Outline each blood parasite and name the species.
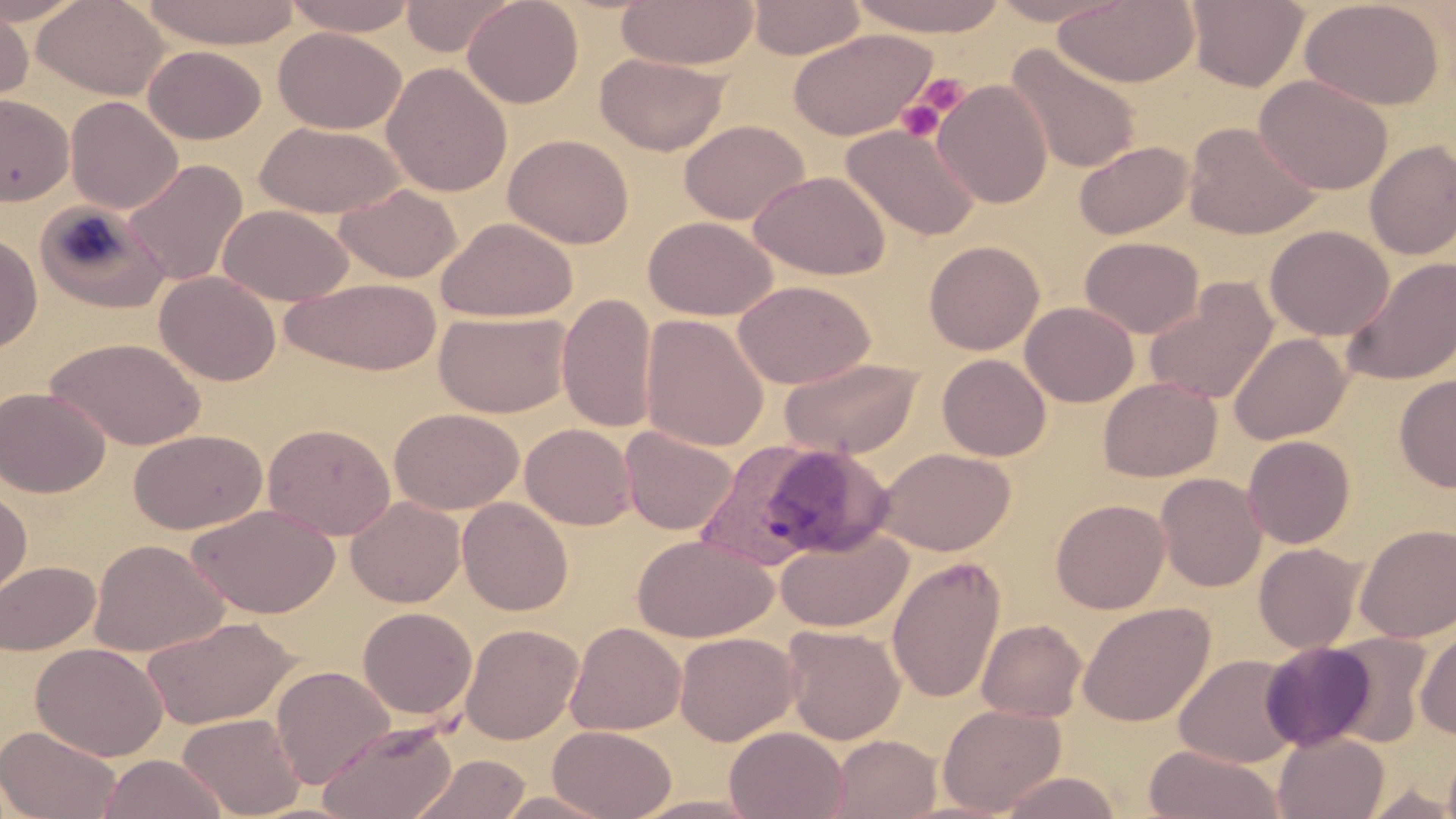
Approximate bounding boxes as (x1,y1)-(x2,y2) corner pairs in pixels.
Plasmodium vivax-infected red blood cells: (694,439)-(872,571).
No Plasmodium falciparum, Plasmodium ovale, Plasmodium malariae, Babesia divergens, or Trypanosoma brucei observed.

Summary:
  - Uninfected red blood cell locations: (0,0)-(88,25), (33,0)-(170,101), (140,0)-(303,48), (280,0)-(419,36), (401,0)-(516,56), (462,0)-(583,108), (616,0)-(759,70), (747,0)-(866,59), (847,0)-(1011,37), (985,0)-(1131,26), (1052,0)-(1200,87), (1186,0)-(1308,90), (1300,0)-(1445,110), (0,8)-(33,110), (274,27)-(406,134), (787,28)-(938,142), (1006,44)-(1142,174), (143,45)-(266,144), (596,53)-(731,155), (382,62)-(512,197), (1255,75)-(1393,194), (933,80)-(1053,209), (0,94)-(74,206), (65,96)-(182,214), (679,119)-(809,224), (254,121)-(406,218), (1183,121)-(1322,239), (840,123)-(983,241), (504,134)-(634,248), (1073,140)-(1193,240), (1364,141)-(1456,260), (123,159)-(248,287), (749,170)-(891,280), (333,183)-(463,283), (34,201)-(169,313), (218,204)-(354,306), (643,216)-(776,320), (435,217)-(578,322), (1265,225)-(1394,341), (0,231)-(42,354), (1080,236)-(1204,338), (924,240)-(1044,355), (1342,256)-(1456,386), (154,271)-(281,386), (280,277)-(443,375), (1143,279)-(1279,405), (733,280)-(876,388), (557,293)-(657,433), (1020,301)-(1139,407), (435,310)-(571,418), (639,314)-(769,452), (1230,332)-(1352,444), (45,336)-(206,451), (937,354)-(1051,460), (778,357)-(924,459), (1395,373)-(1456,492), (1098,377)-(1222,481), (0,386)-(110,498), (389,407)-(523,515), (263,423)-(395,540), (521,423)-(636,530), (620,426)-(738,536), (129,429)-(267,534), (1242,435)-(1356,549), (875,447)-(1015,556), (1155,472)-(1267,592), (0,487)-(33,609), (346,496)-(465,607), (457,497)-(573,615), (1050,498)-(1170,613), (187,503)-(341,618), (1355,522)-(1456,642), (775,528)-(912,633), (632,534)-(778,643), (88,539)-(227,657), (1254,543)-(1366,654), (887,555)-(1007,703), (0,560)-(99,655), (1077,602)-(1215,727), (358,607)-(477,720), (142,615)-(300,729), (977,618)-(1087,722), (565,622)-(686,736), (460,623)-(583,744), (782,625)-(905,745), (1415,625)-(1456,739), (674,631)-(799,746), (1328,632)-(1432,746), (31,641)-(168,760), (1260,641)-(1376,751), (1174,654)-(1302,768), (271,665)-(394,788), (937,704)-(1066,816), (177,712)-(305,818), (317,719)-(459,819), (0,725)-(122,819), (548,725)-(677,819), (724,726)-(848,819), (1273,732)-(1390,819), (829,734)-(942,819), (1443,742)-(1456,819), (1143,745)-(1285,819), (405,751)-(534,818), (99,754)-(228,818), (997,771)-(1124,819), (1360,785)-(1456,818), (492,790)-(618,818), (625,794)-(767,818)
  - Platelet locations: (911,75)-(970,122), (896,86)-(955,141)
  - Slide-level diagnosis: Plasmodium vivax
  - Preparation: thin blood smear
  - Modality: optical microscopy
  - Image size: 1456×819 pixels
  - Stain: May-Grünwald-Giemsa
  - Field of view: single
  - Magnification: 1000x